Classify this cell by malaria status.
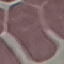
Uninfected.

{
  "image_type": "automatically extracted cell patch, resized to 64 × 64 pixels",
  "preparation": "thin blood film",
  "stain": "Giemsa",
  "capture": "smartphone through the microscope eyepiece"
}